Assess the morphology of the erythrocytes.
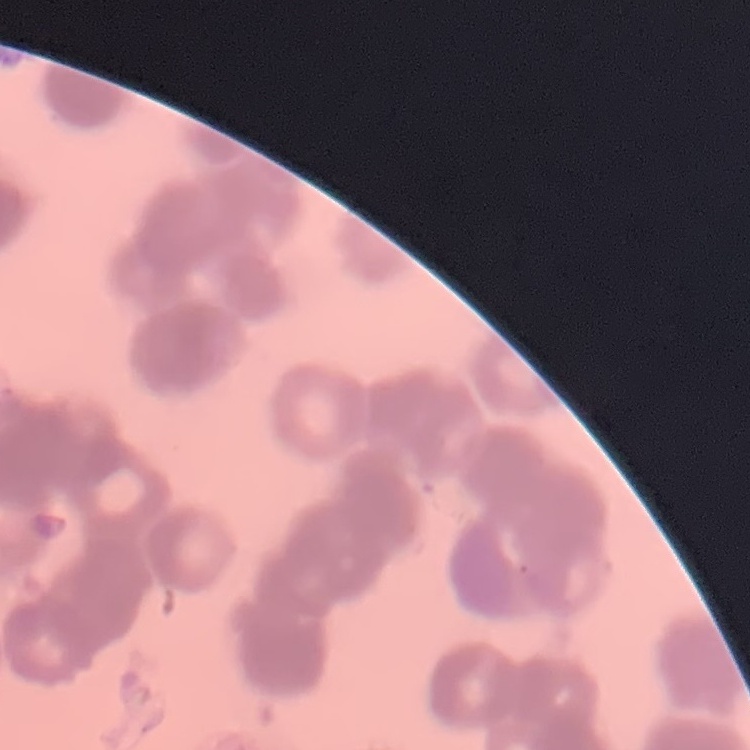

Rouleaux formation.

Stained with either Field's or Giemsa. Square crop of a larger photomicrograph. Thin blood film.